Identify the preparation type.
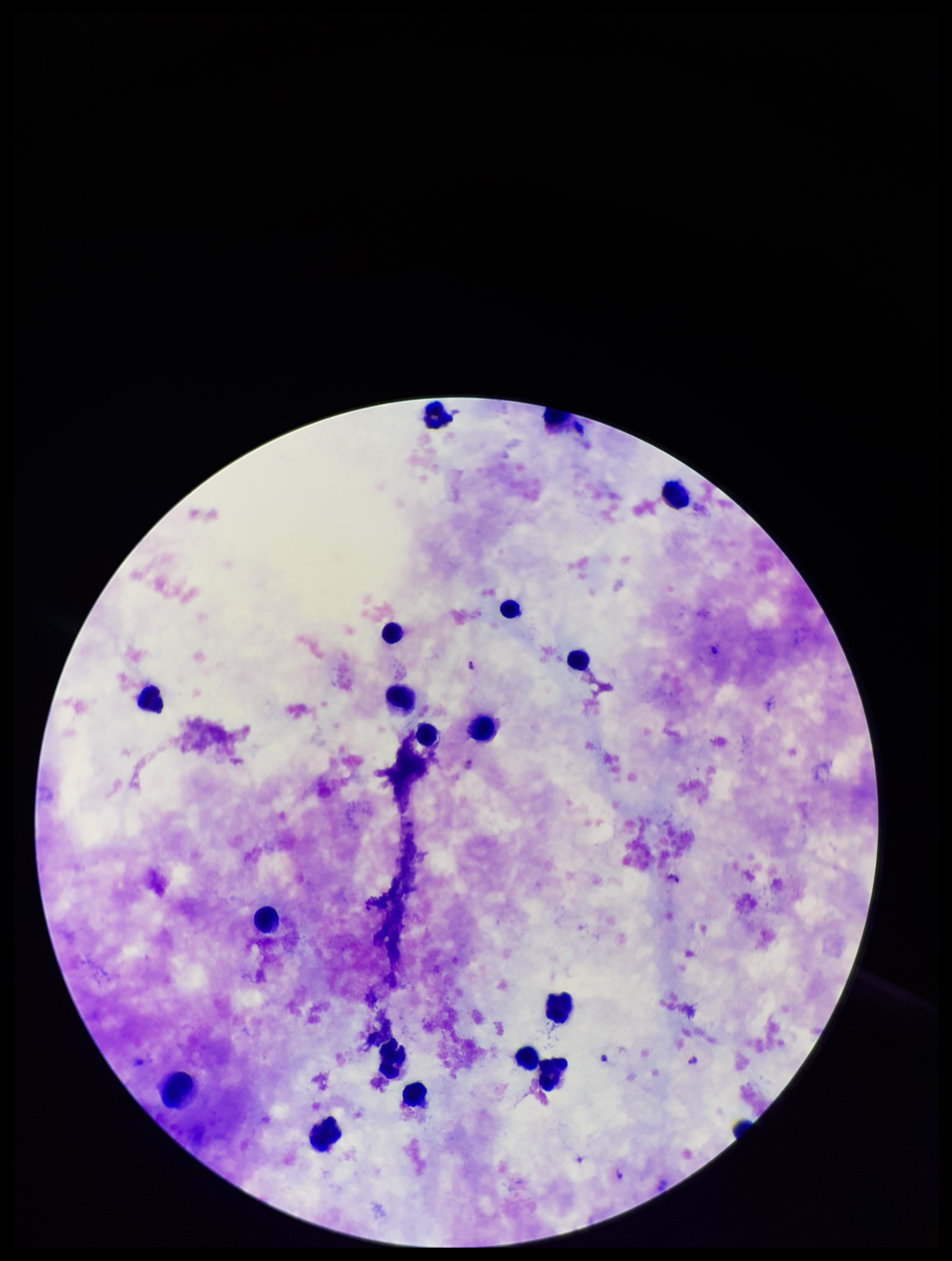
Thick.

species reported for this patient = Plasmodium falciparum
image size = 952×1261 pixels
patient malaria status = positive
leukocyte count = 19
parasite count = 1
field of view = one from this slide
capture = smartphone photograph through the microscope eyepiece
stain = Giemsa
Plasmodium parasites = identified